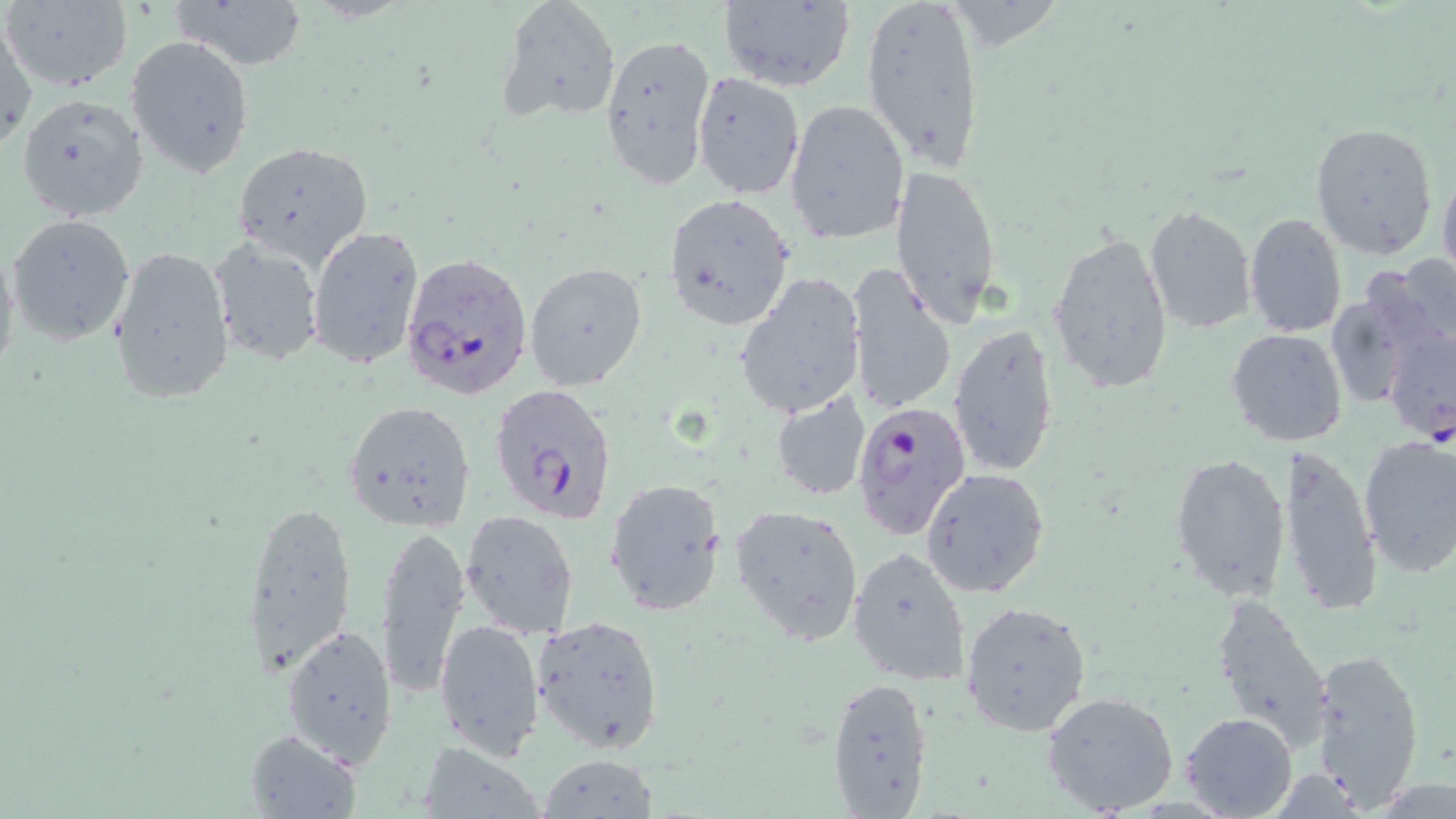

Summary:
  - Coordinate format: approximate bounding boxes as [x1, y1, x2, y2] in pixels
  - Uninfected red blood cell locations: [5, 0, 132, 92], [173, 0, 307, 71], [498, 0, 622, 123], [718, 0, 856, 93], [861, 0, 986, 171], [0, 18, 36, 150], [599, 31, 716, 190], [126, 38, 254, 177], [692, 72, 804, 201], [17, 93, 149, 220], [784, 100, 909, 244], [1309, 122, 1439, 262], [231, 141, 372, 267], [888, 161, 1004, 327], [1438, 165, 1456, 287], [664, 192, 796, 331], [1144, 205, 1256, 334], [7, 214, 136, 345], [1244, 214, 1347, 338], [306, 224, 425, 370], [1048, 230, 1173, 396], [0, 232, 22, 388], [210, 237, 325, 366], [107, 245, 233, 405], [1368, 254, 1456, 366], [525, 262, 649, 393], [845, 263, 955, 417], [735, 272, 866, 419], [949, 323, 1060, 479], [1225, 327, 1347, 447], [772, 392, 870, 499], [342, 398, 477, 532], [1357, 434, 1456, 577], [1274, 443, 1381, 617], [1169, 451, 1292, 604], [920, 467, 1050, 598], [604, 477, 727, 617], [238, 499, 355, 682], [730, 503, 866, 647], [459, 510, 580, 641], [374, 524, 469, 699], [848, 544, 971, 686], [1210, 594, 1335, 749], [961, 600, 1092, 737], [532, 613, 665, 755], [435, 618, 544, 763], [280, 621, 398, 766], [1309, 645, 1427, 808], [826, 674, 935, 817], [1042, 689, 1180, 816], [1180, 712, 1298, 819], [242, 728, 363, 819], [416, 742, 546, 818], [537, 754, 659, 819]
  - Plasmodium falciparum-infected red blood cell locations: [398, 250, 532, 400], [1381, 321, 1455, 445], [491, 385, 620, 525], [850, 398, 973, 540]
  - Slide-level diagnosis: Plasmodium falciparum
  - Stain: May-Grünwald-Giemsa
  - Image size: 1456×819 pixels
  - Modality: light microscopy
  - Field of view: one of a larger specimen
  - Preparation: thin blood smear
  - Magnification: 1000x